Assess this cell for malaria.
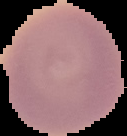

It is uninfected.

{
  "image_type": "cell region segmented out of the field of view; surrounding area masked to black",
  "preparation": "thin blood smear",
  "image_size": "127×136 pixels"
}